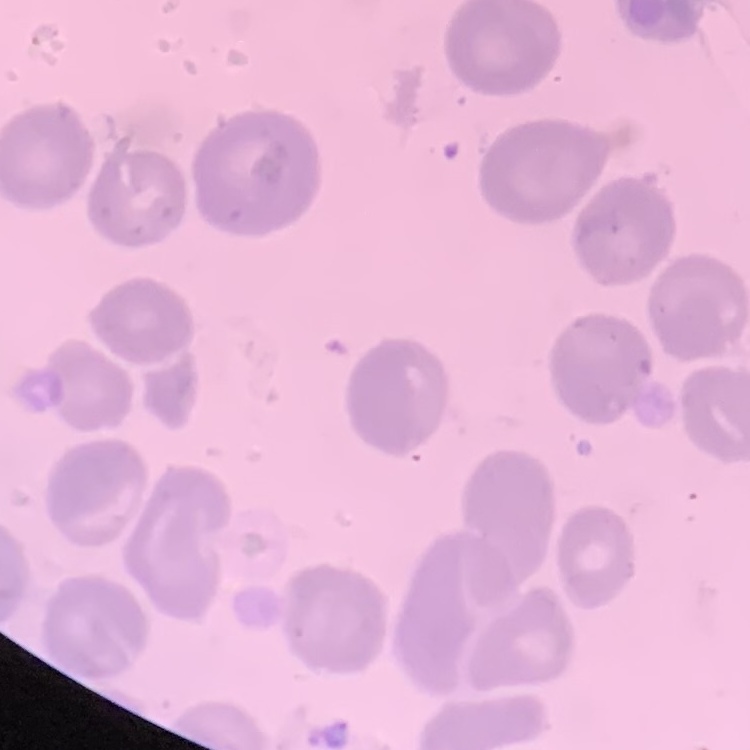 The red blood cells show no rouleaux formation. Stained with either Field's or Giemsa. Thin blood smear. Square crop of a larger photomicrograph.